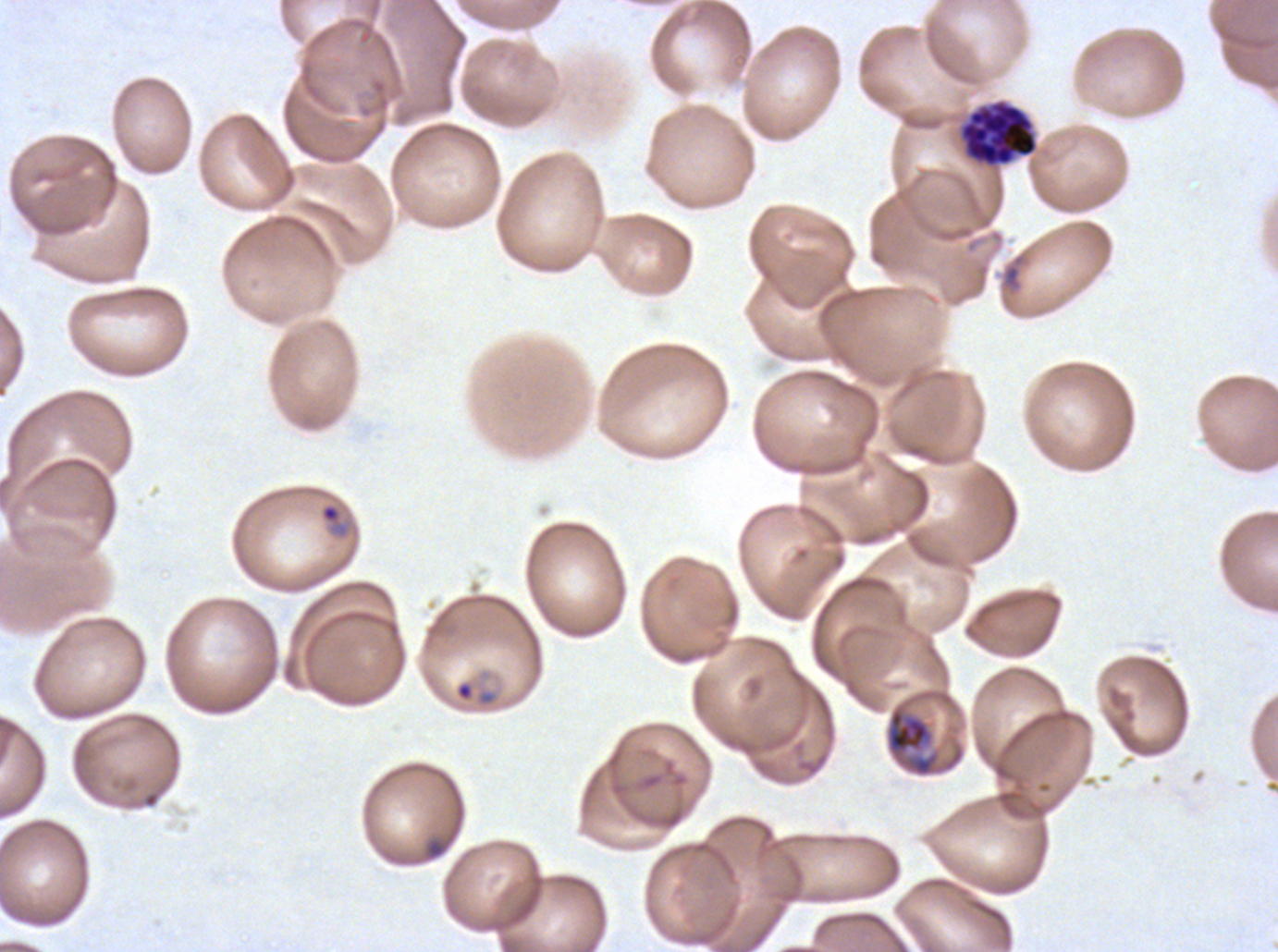
Approximate bounding rectangles given as corner coordinates in pixels from the top-left.
Summary:
  - Segmenter locations: (x1=961, y1=102, x2=1038, y2=166)
  - Early schizont locations: (x1=884, y1=702, x2=965, y2=778)
  - Ring locations: (x1=319, y1=502, x2=350, y2=539), (x1=455, y1=680, x2=474, y2=702), (x1=424, y1=837, x2=448, y2=860)
  - Stain: Giemsa
  - Field of view: sub-image separated from a larger composite
  - Life-cycle stages observed: ring, early schizont, segmenter
  - Preparation: thin blood smear
  - Specimen: ex-vivo Plasmodium falciparum culture from a patient in The Gambia, grown for 24 to 48 hours
  - Image size: 1278×952 pixels